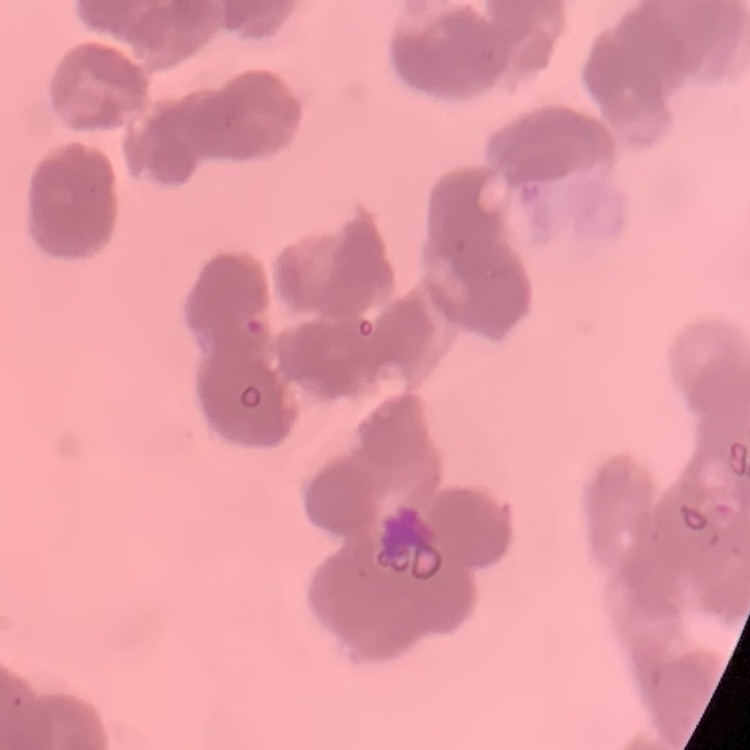
Summary:
  - Red blood cell morphology: rouleaux formation
  - Preparation: thin blood film
  - Image type: one tile cut from a larger photomicrograph
  - Stain: Field's or Giemsa